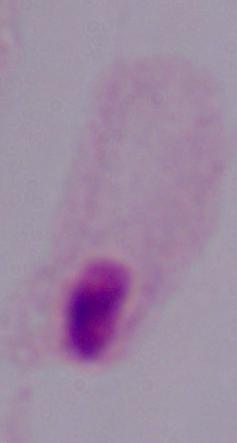 A trichomonad is shown. Micrograph. 1000x magnification.